Assess this cell for malaria.
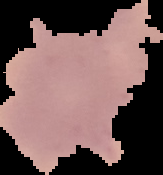

It is uninfected.

Image is 163×175 pixels. Segmented cell region on a black background. From a thin blood film.